Assess the morphology of the erythrocytes.
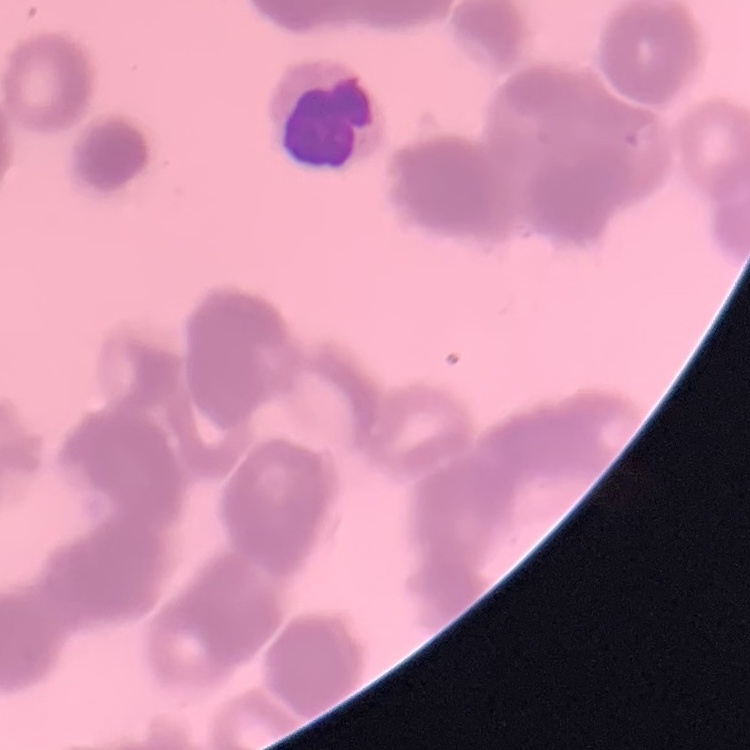

Rouleaux formation.

Summary:
  - Stain: Field's or Giemsa
  - Image type: one tile cut from a larger photomicrograph
  - Preparation: thin blood smear